Report the malaria status of this cell.
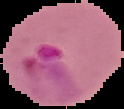

It is parasitized.

Summary:
  - Image size: 124×109 pixels
  - Preparation: thin blood film
  - Image type: cell region segmented out of the field of view; surrounding area masked to black